Assess the morphology of the erythrocytes.
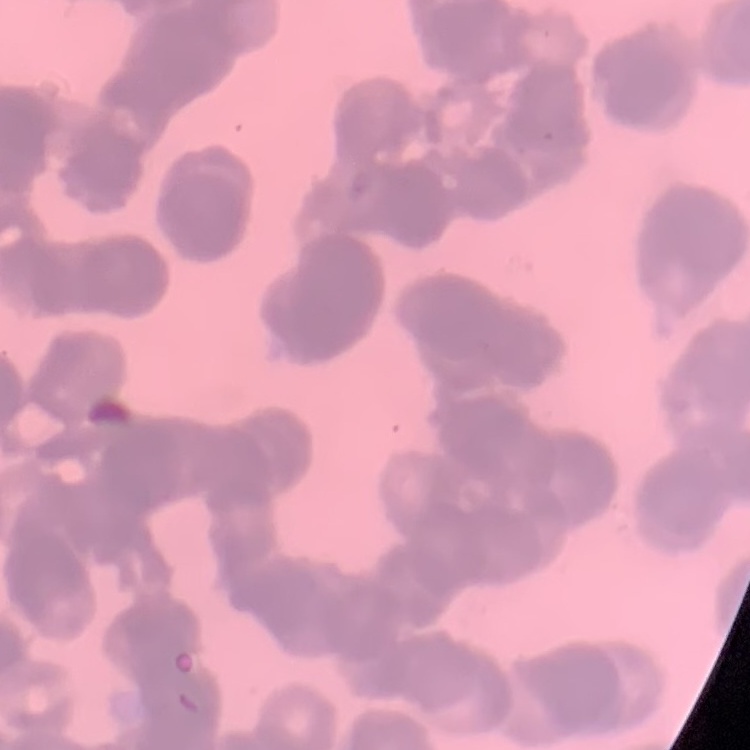

They show rouleaux formation.

Thin peripheral smear. Square crop of a larger photomicrograph. Stained with either Field's or Giemsa.